Assess this cell for malaria.
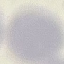

Uninfected.

preparation = thin blood film
stain = Giemsa
image type = cell patch, automatically extracted from a larger field of view and resized to 64 × 64 pixels
capture = smartphone through the microscope eyepiece